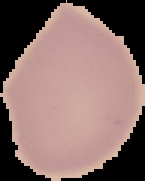

preparation = thin blood film
image type = cell region segmented out of the field of view; surrounding area masked to black
image size = 145×181 pixels
malaria status = uninfected